Name the blood parasite species.
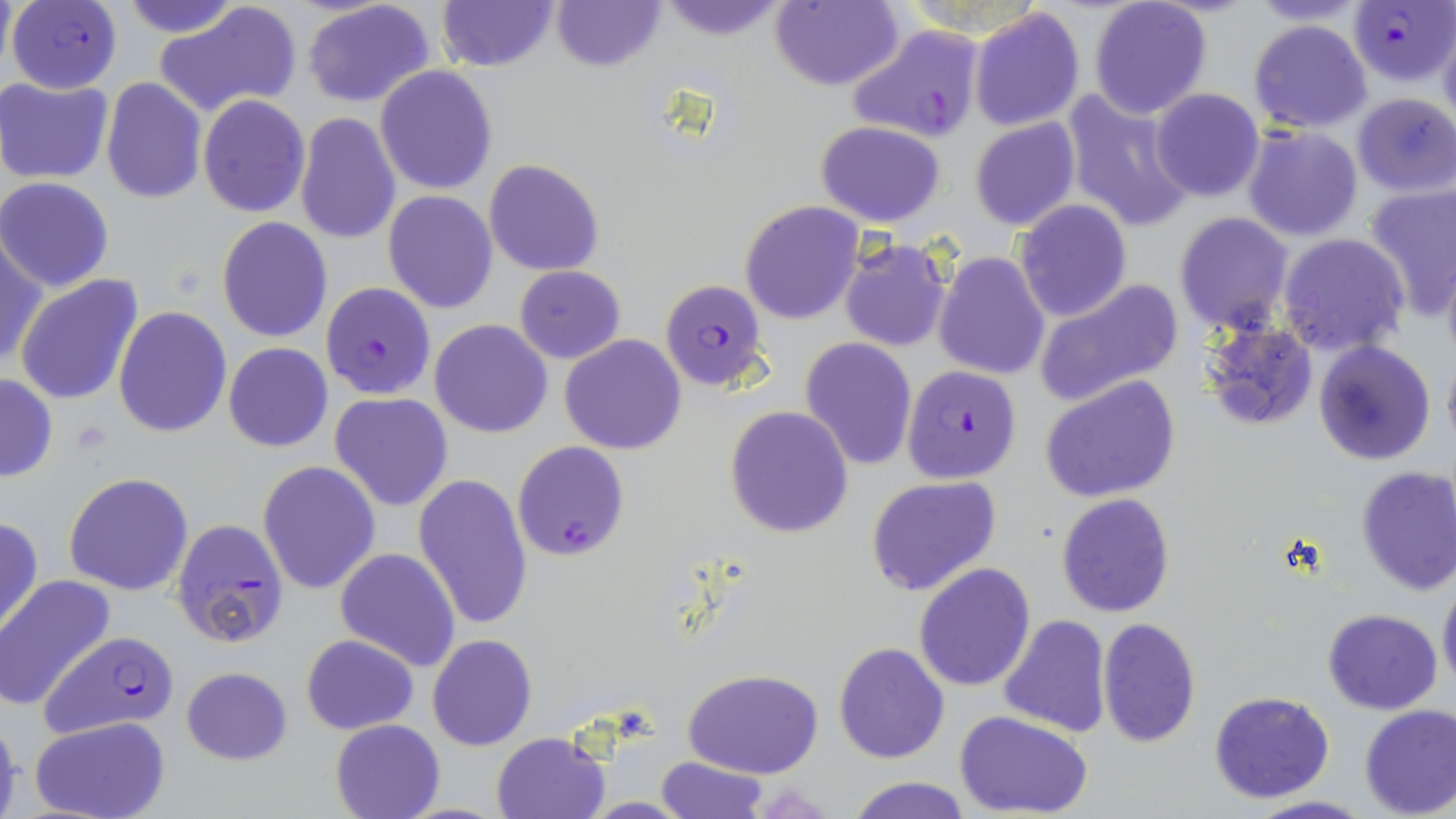

Plasmodium falciparum.

Approximate bounding boxes as (x1, y1, x2, y2) in pixels. Plasmodium falciparum-infected red blood cell locations: (1349, 0, 1455, 86), (5, 1, 122, 93), (844, 22, 989, 146), (661, 278, 770, 392), (320, 282, 436, 400), (902, 364, 1022, 484), (513, 439, 630, 562), (170, 517, 291, 648), (40, 630, 180, 739). Uninfected red blood cell locations: (123, 0, 243, 37), (301, 0, 438, 109), (436, 0, 558, 73), (551, 0, 664, 72), (653, 0, 791, 40), (1088, 0, 1214, 120), (153, 2, 302, 120), (767, 2, 903, 90), (968, 6, 1086, 132), (1247, 18, 1374, 134), (1438, 21, 1456, 130), (374, 65, 497, 195), (1, 77, 113, 185), (100, 78, 207, 205), (1149, 88, 1266, 202), (1062, 90, 1195, 235), (1352, 93, 1456, 197), (197, 94, 311, 216), (294, 111, 402, 247), (969, 118, 1079, 232), (814, 120, 947, 228), (1242, 123, 1364, 241), (483, 159, 604, 276), (0, 177, 116, 292), (1362, 182, 1456, 320), (383, 190, 498, 314), (738, 200, 865, 325), (1014, 201, 1133, 322), (1173, 212, 1294, 338), (216, 216, 333, 343), (0, 232, 46, 369), (1277, 232, 1410, 358), (838, 237, 953, 352), (933, 252, 1051, 378), (1441, 259, 1456, 366), (514, 266, 625, 364), (14, 274, 146, 408), (1032, 277, 1184, 407), (114, 306, 232, 438), (429, 318, 554, 438), (1200, 320, 1319, 429), (559, 334, 687, 456), (801, 336, 919, 470), (1313, 340, 1436, 465), (223, 342, 333, 452), (1443, 351, 1456, 454), (0, 373, 57, 482), (1040, 374, 1181, 502), (329, 392, 453, 512), (724, 405, 853, 539), (256, 461, 382, 596), (1354, 465, 1456, 595), (64, 471, 194, 596), (411, 472, 534, 630), (865, 476, 1003, 597), (1056, 492, 1176, 618), (0, 516, 43, 639), (334, 548, 462, 672), (914, 563, 1036, 691), (1438, 576, 1456, 694), (0, 577, 115, 711), (1321, 608, 1444, 713), (998, 614, 1111, 739), (1096, 618, 1201, 748), (300, 633, 420, 735), (428, 634, 537, 751), (834, 642, 949, 764), (181, 666, 292, 765), (682, 668, 824, 779), (1208, 690, 1336, 804), (1358, 704, 1456, 819), (955, 711, 1095, 818), (0, 712, 23, 818), (29, 718, 171, 818), (331, 718, 444, 819), (491, 731, 610, 819), (657, 755, 768, 819), (842, 777, 975, 819), (1243, 795, 1375, 819). Thin blood film. Image is 1456×819 pixels. Optical microscopy. May-Grünwald-Giemsa-stained preparation. 1000x magnification. Single field of view.